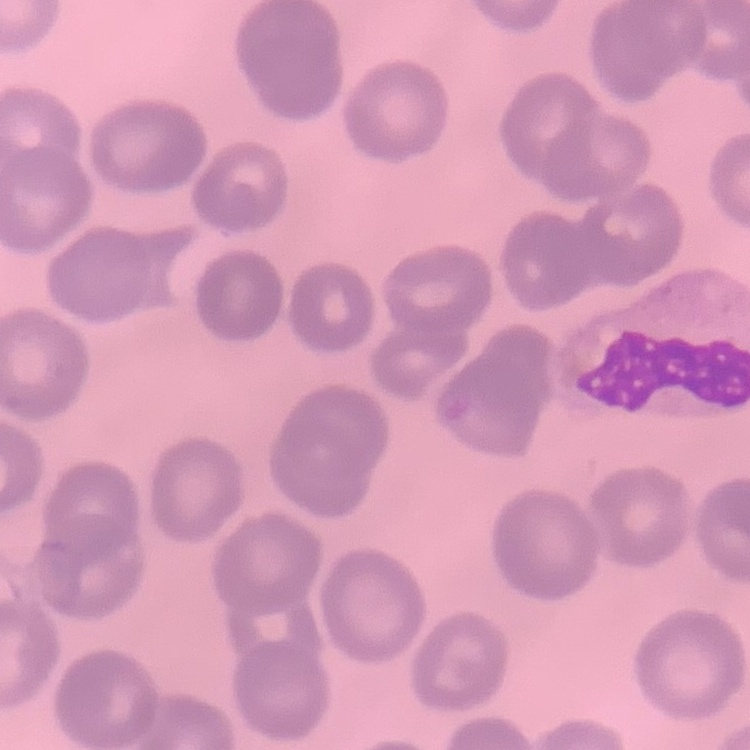
erythrocyte morphology = no rouleaux formation
preparation = thin peripheral smear
image type = square crop of a larger photomicrograph
stain = Field's or Giemsa